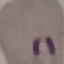

Summary:
  - Result: malaria parasites detected
  - Capture: smartphone camera at the microscope eyepiece
  - Stain: Giemsa
  - Preparation: thin smear
  - Image type: cell patch, automatically extracted from a larger field of view and resized to 64 × 64 pixels